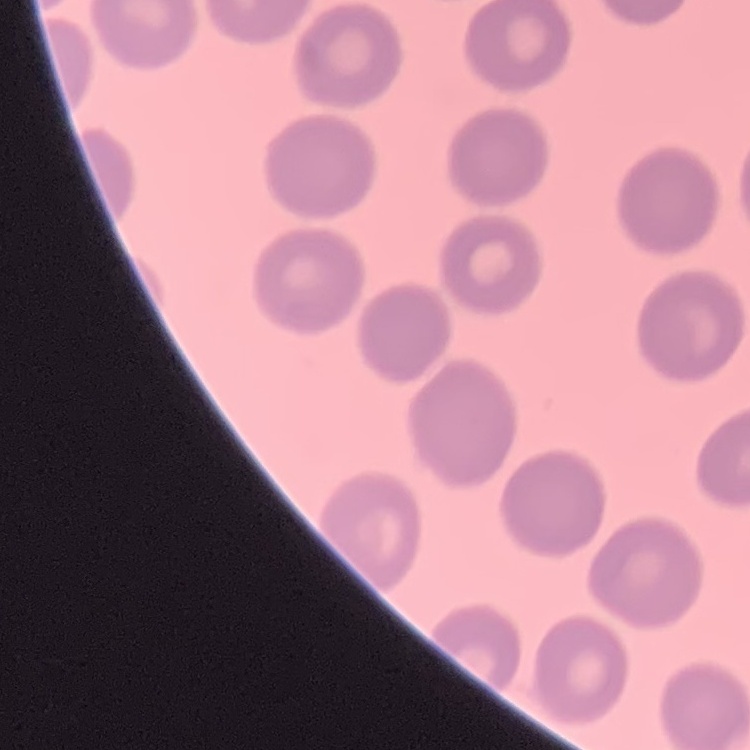

The red blood cells exhibit no rouleaux formation. Stained with either Field's or Giemsa. One tile cut from a larger photomicrograph. Thin blood smear.